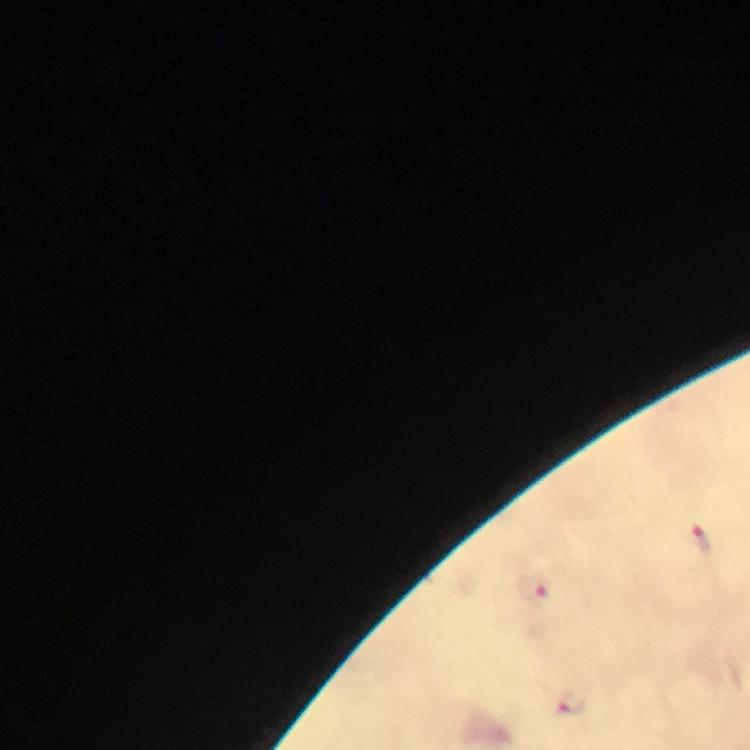 Approximate centers as [x, y] in pixels. Plasmodium parasite locations: [702, 538], [533, 587], [571, 702]. At 100x magnification. A crop from one field of view. Photographed with a smartphone mounted on the microscope. From a diagnostic examination for malaria. Thick blood smear. Immersion oil was used. Image is 750×750 pixels. Giemsa stain.